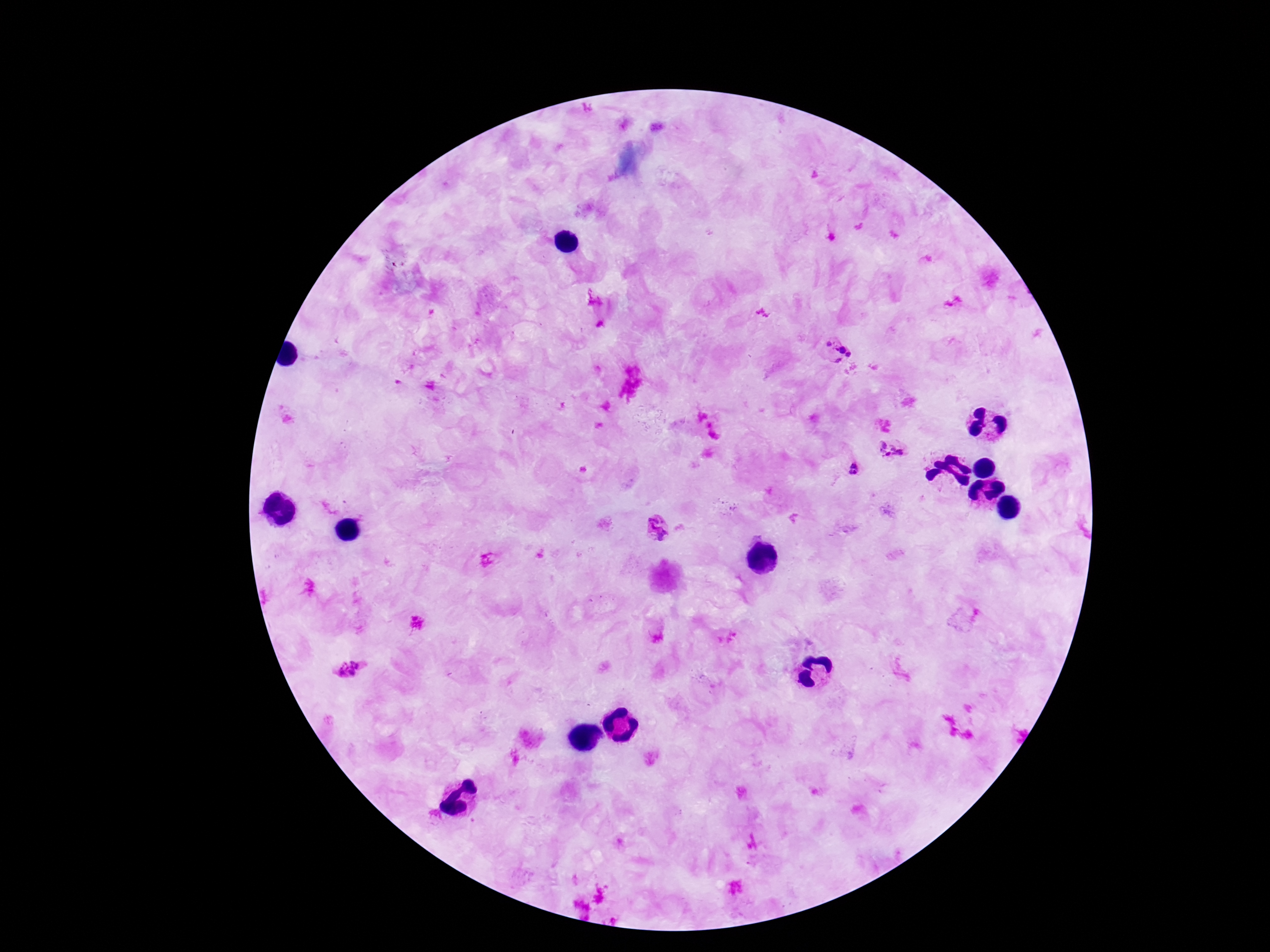

magnification = 100x
capture = smartphone camera through the microscope eyepiece
patient malaria status = positive
preparation = thick blood smear
stain = Giemsa
field of view = one from this slide
Plasmodium parasite locations = approximate centers as (x, y) in pixels: (827, 344), (840, 348), (849, 355), (838, 360), (892, 451), (855, 469), (657, 528), (351, 668)
image size = 1270×952 pixels